Give the extent of all Plasmodium falciparum-infected red blood cells.
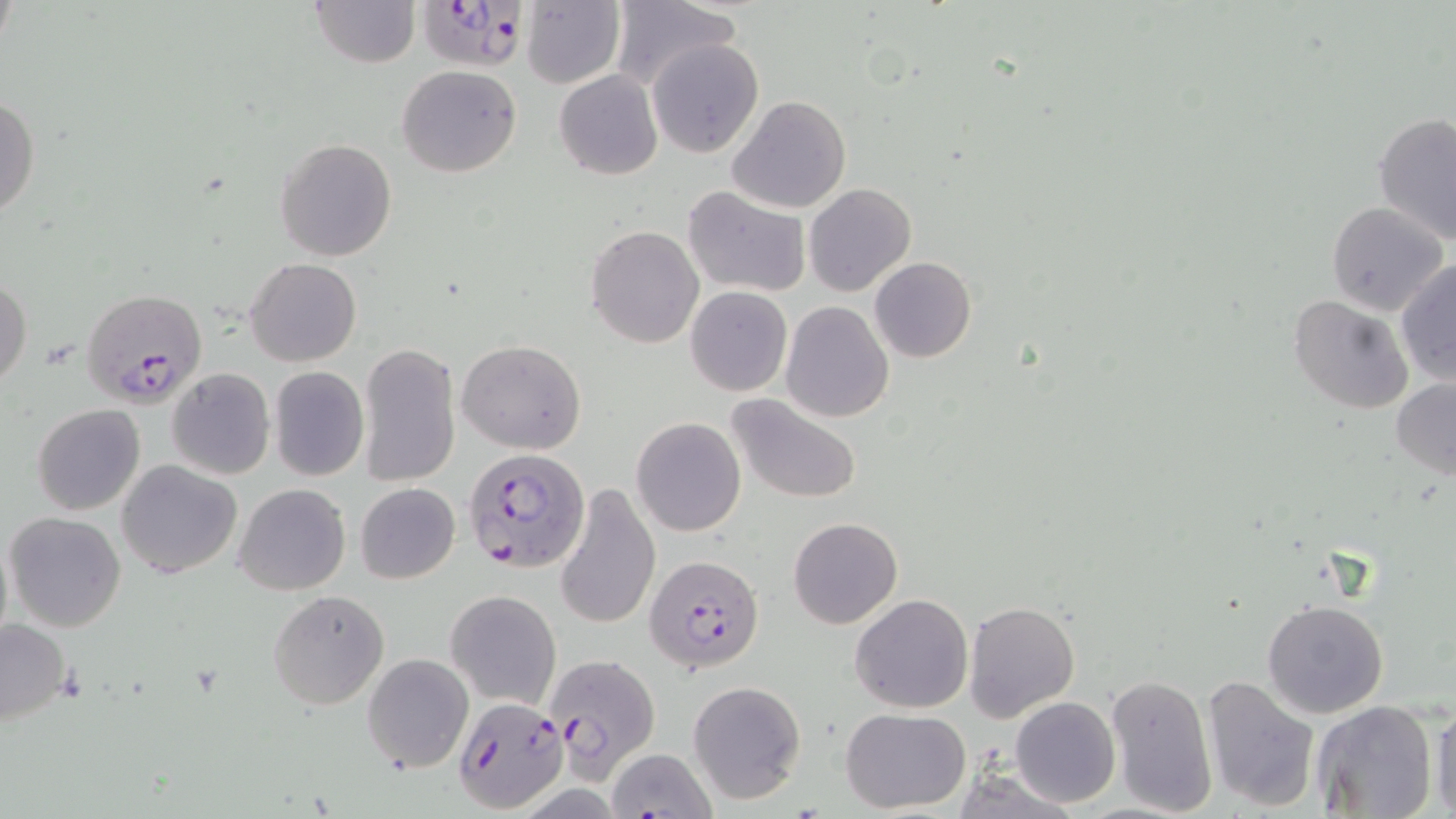
Approximate bounding boxes as [x1, y1, x2, y2] in pixels.
Plasmodium falciparum-infected red blood cells: [418, 0, 532, 71], [82, 288, 208, 410], [464, 449, 590, 574], [646, 555, 765, 674], [542, 651, 661, 778], [452, 696, 569, 812].

slide-level diagnosis = Plasmodium falciparum
preparation = thin blood film
magnification = 1000x
modality = light microscopy
uninfected red blood cell locations = approximate bounding boxes as [x1, y1, x2, y2] in pixels: [310, 0, 419, 68], [521, 0, 626, 88], [607, 1, 743, 92], [647, 38, 764, 157], [397, 64, 521, 178], [554, 70, 662, 179], [0, 92, 40, 222], [728, 95, 852, 215], [1373, 113, 1456, 246], [275, 138, 397, 260], [804, 184, 915, 296], [682, 186, 810, 298], [1327, 202, 1448, 317], [587, 225, 704, 348], [869, 256, 977, 363], [245, 258, 361, 367], [1395, 259, 1456, 387], [813, 273, 917, 397], [0, 275, 31, 390], [686, 286, 792, 396], [1289, 293, 1413, 414], [782, 300, 894, 423], [456, 339, 587, 454], [358, 343, 461, 488], [166, 367, 276, 480], [269, 367, 370, 480], [1391, 377, 1456, 481], [726, 394, 863, 504], [31, 403, 145, 516], [630, 417, 746, 537], [116, 459, 242, 578], [355, 482, 461, 585], [554, 482, 660, 632], [234, 483, 351, 596], [6, 511, 126, 631], [788, 517, 902, 629], [0, 521, 14, 652], [799, 548, 932, 698], [267, 590, 390, 711], [445, 590, 561, 710], [851, 594, 973, 713], [965, 600, 1080, 722], [1262, 600, 1387, 718], [0, 619, 73, 728], [361, 652, 474, 773], [1105, 673, 1218, 817], [1201, 674, 1321, 809], [687, 680, 807, 806], [1010, 696, 1120, 807], [1311, 700, 1439, 819], [1429, 704, 1456, 818], [840, 709, 970, 813], [607, 747, 716, 819]
image size = 1456×819 pixels
field of view = single
stain = May-Grünwald-Giemsa